State which parasite is depicted.
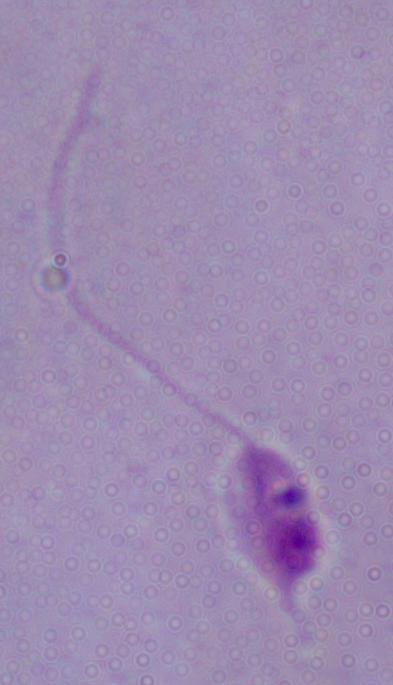

This is Leishmania.

1000x magnification. Micrograph.